Classify this cell by malaria status.
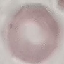
Uninfected.

Summary:
  - Image type: automatically extracted cell patch, resized to 64 × 64 pixels
  - Preparation: thin smear
  - Stain: Giemsa
  - Capture: smartphone camera at the microscope eyepiece